State the preparation type.
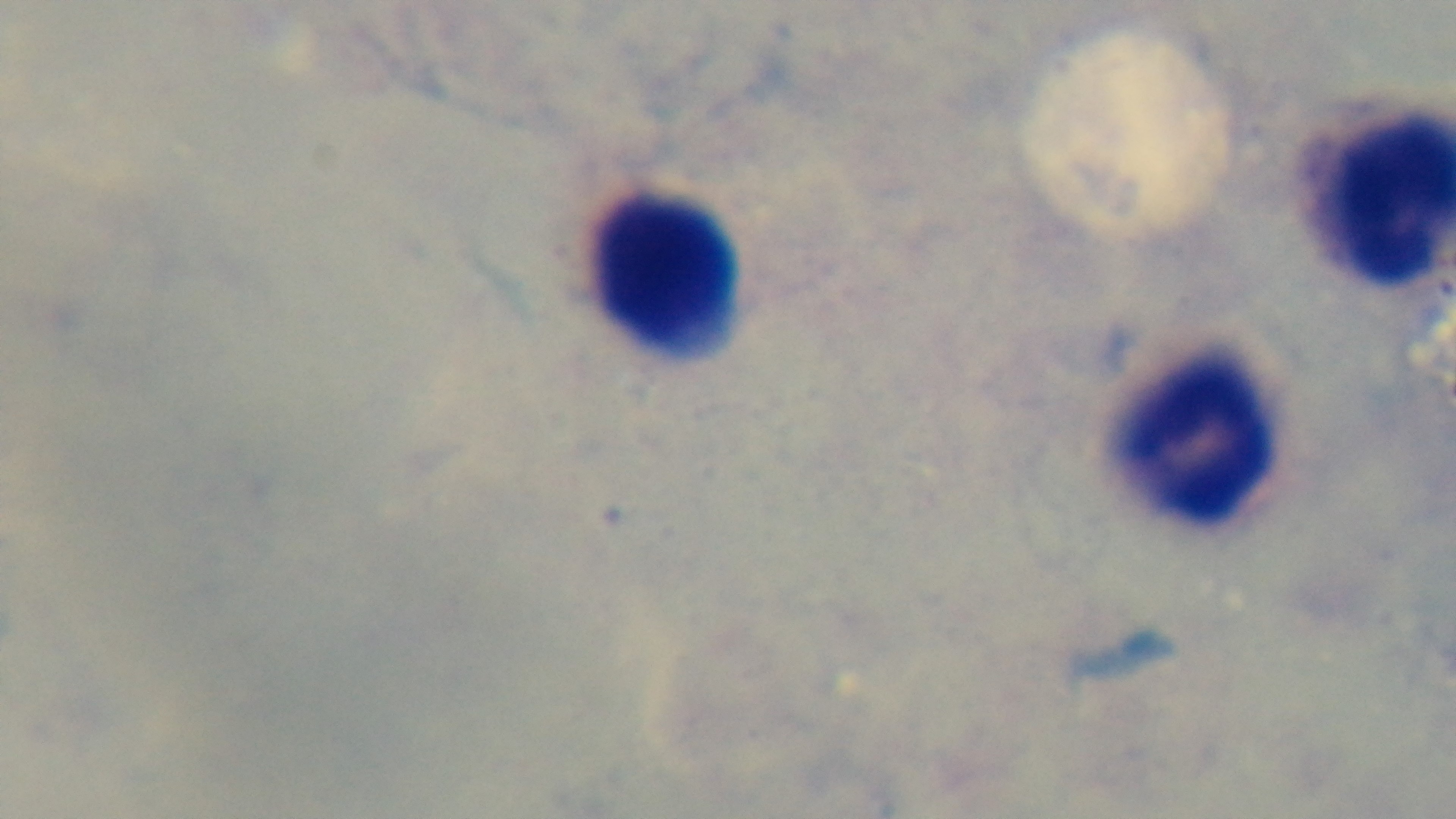

A thick smear.

{
  "objective": "100x oil immersion",
  "malaria_status": "negative",
  "modality": "light microscopy",
  "capture": "mounted 4K digital camera",
  "stain": "Giemsa",
  "field_of_view": "single"
}